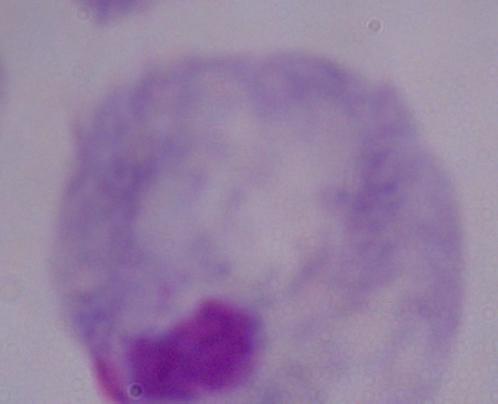

magnification = 1000x
identification = trichomonad
modality = micrograph